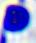 Micrograph. A white blood cell is seen. Captured at 400x magnification.